Assess the morphology of the red blood cells.
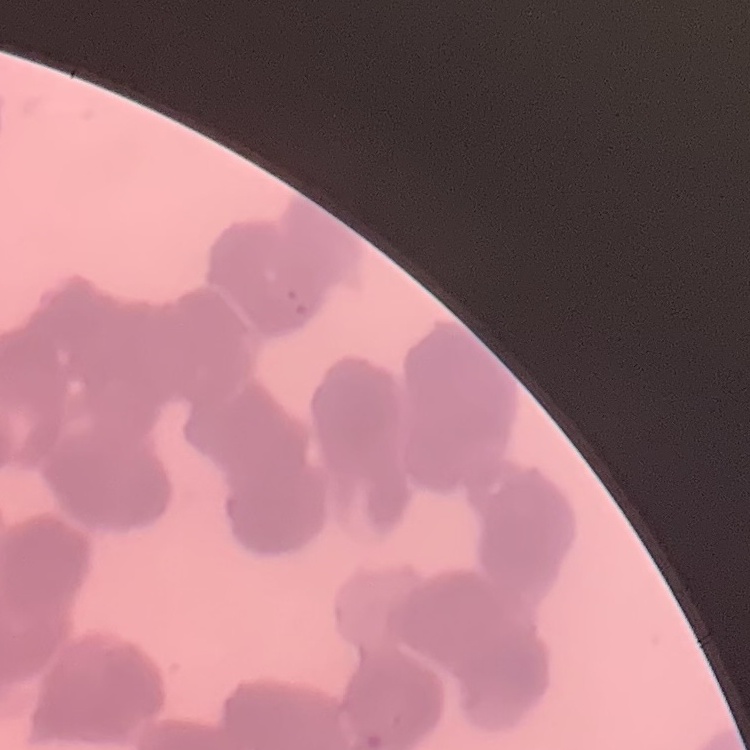

They show rouleaux formation.

Summary:
  - Image type: square crop of a larger photomicrograph
  - Stain: Field's or Giemsa
  - Preparation: thin blood film